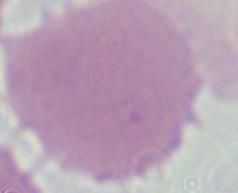
magnification = 1000x
modality = photomicrograph
identification = erythrocyte